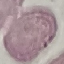

Summary:
  - Result: no malaria parasites detected
  - Preparation: thin blood film
  - Stain: Giemsa
  - Capture: smartphone camera at the microscope eyepiece
  - Image type: automatically extracted cell patch, resized to 64 × 64 pixels